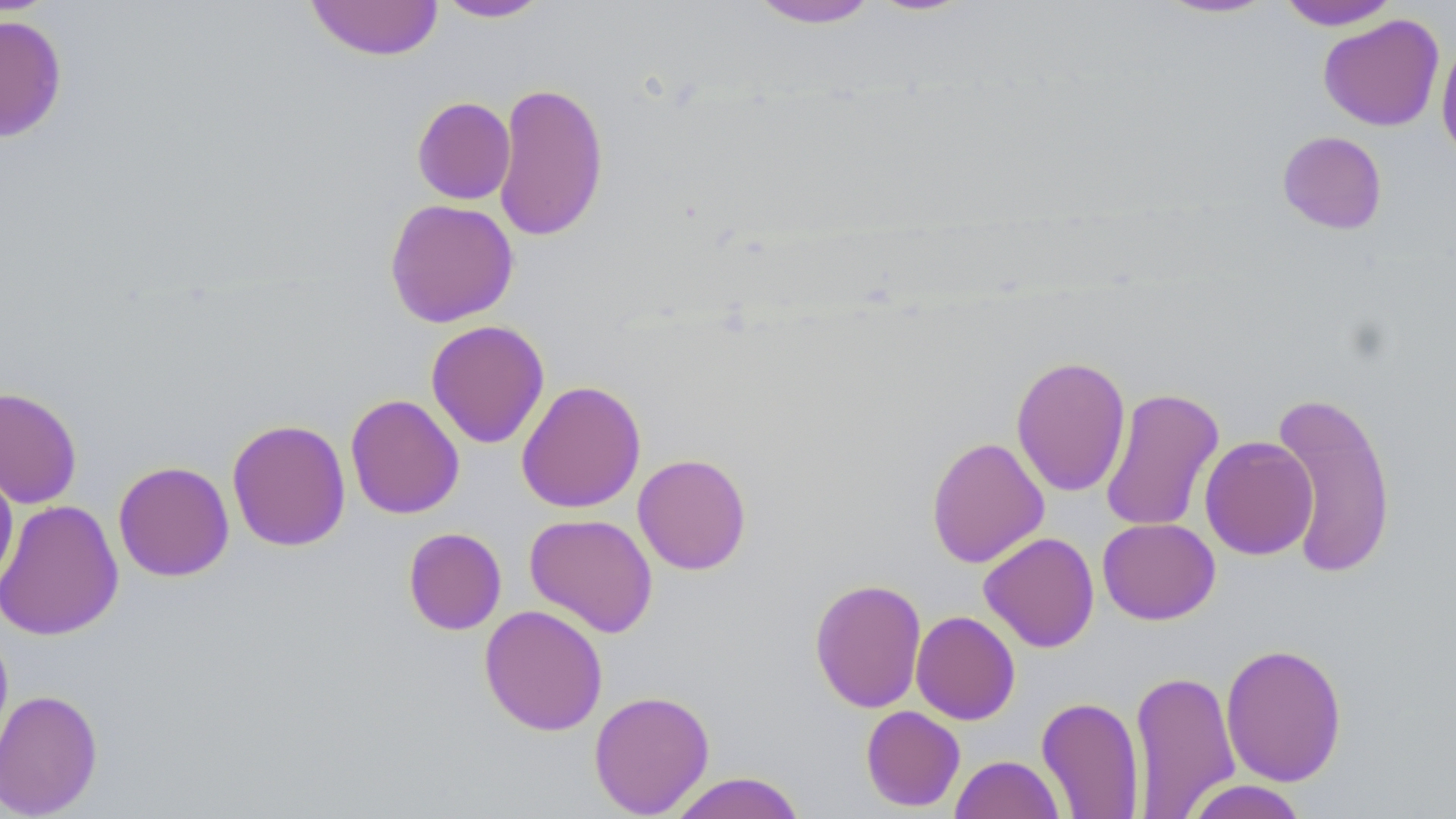
{
  "slide_level_diagnosis": "negative for blood parasites",
  "modality": "optical microscopy",
  "preparation": "thin blood smear",
  "image_size": "1456×819 pixels",
  "magnification": "1000x",
  "stain": "May-Grünwald-Giemsa",
  "field_of_view": "single",
  "uninfected_red_blood_cell_locations": "approximate bounding boxes as (x1,y1)-(x2,y2) corner pairs in pixels: (305,0)-(445,61), (434,0)-(553,22), (747,0)-(881,28), (863,0)-(979,17), (1152,0)-(1282,20), (1276,1)-(1401,30), (0,14)-(68,142), (1317,14)-(1445,132), (1436,38)-(1456,165), (492,81)-(609,241), (412,97)-(515,205), (1277,131)-(1387,235), (384,198)-(519,328), (425,320)-(550,449), (1010,355)-(1131,497), (516,379)-(646,513), (0,386)-(83,509), (1100,387)-(1224,533), (1270,388)-(1397,580), (345,394)-(465,519), (226,418)-(351,552), (1200,435)-(1319,560), (926,436)-(1050,569), (632,453)-(752,575), (0,459)-(19,595), (113,461)-(234,581), (0,499)-(124,641), (524,513)-(658,638), (1097,517)-(1220,625), (403,527)-(506,635), (979,532)-(1100,652), (809,577)-(927,713), (479,604)-(608,736), (910,611)-(1021,725), (0,621)-(14,766), (1220,642)-(1347,787), (1129,668)-(1240,817), (0,688)-(103,818), (588,689)-(715,818), (1036,696)-(1145,818), (860,705)-(965,812), (950,754)-(1066,818), (668,771)-(806,819), (1181,780)-(1310,818)"
}